Comment on the morphology of the erythrocytes.
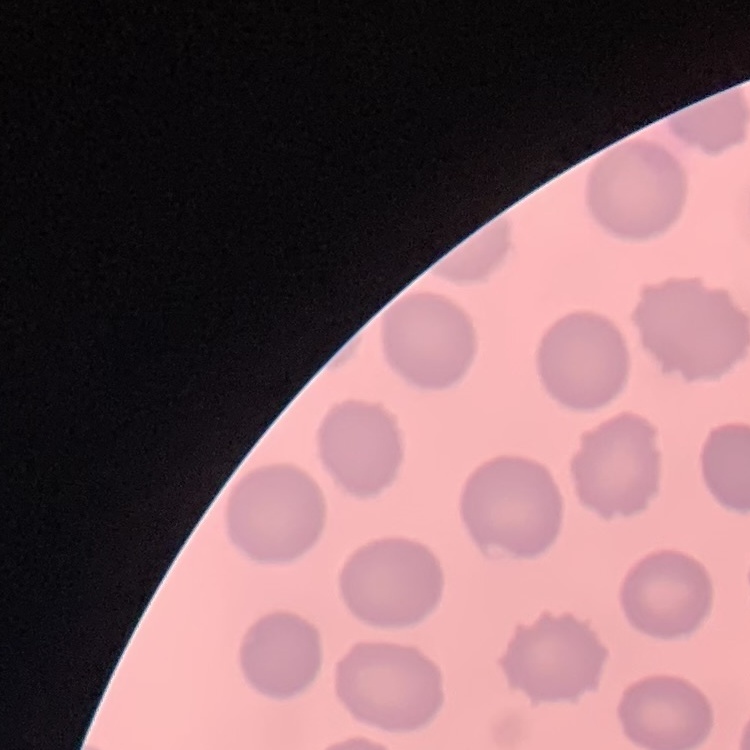

No rouleaux formation.

Summary:
  - Preparation: thin blood smear
  - Image type: one tile cut from a larger photomicrograph
  - Stain: Field's or Giemsa